Assess this cell for malaria.
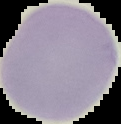
It is uninfected.

Summary:
  - Image type: cell region segmented out of the field of view; surrounding area masked to black
  - Image size: 121×124 pixels
  - Preparation: thin blood smear